Locate and identify every blood parasite.
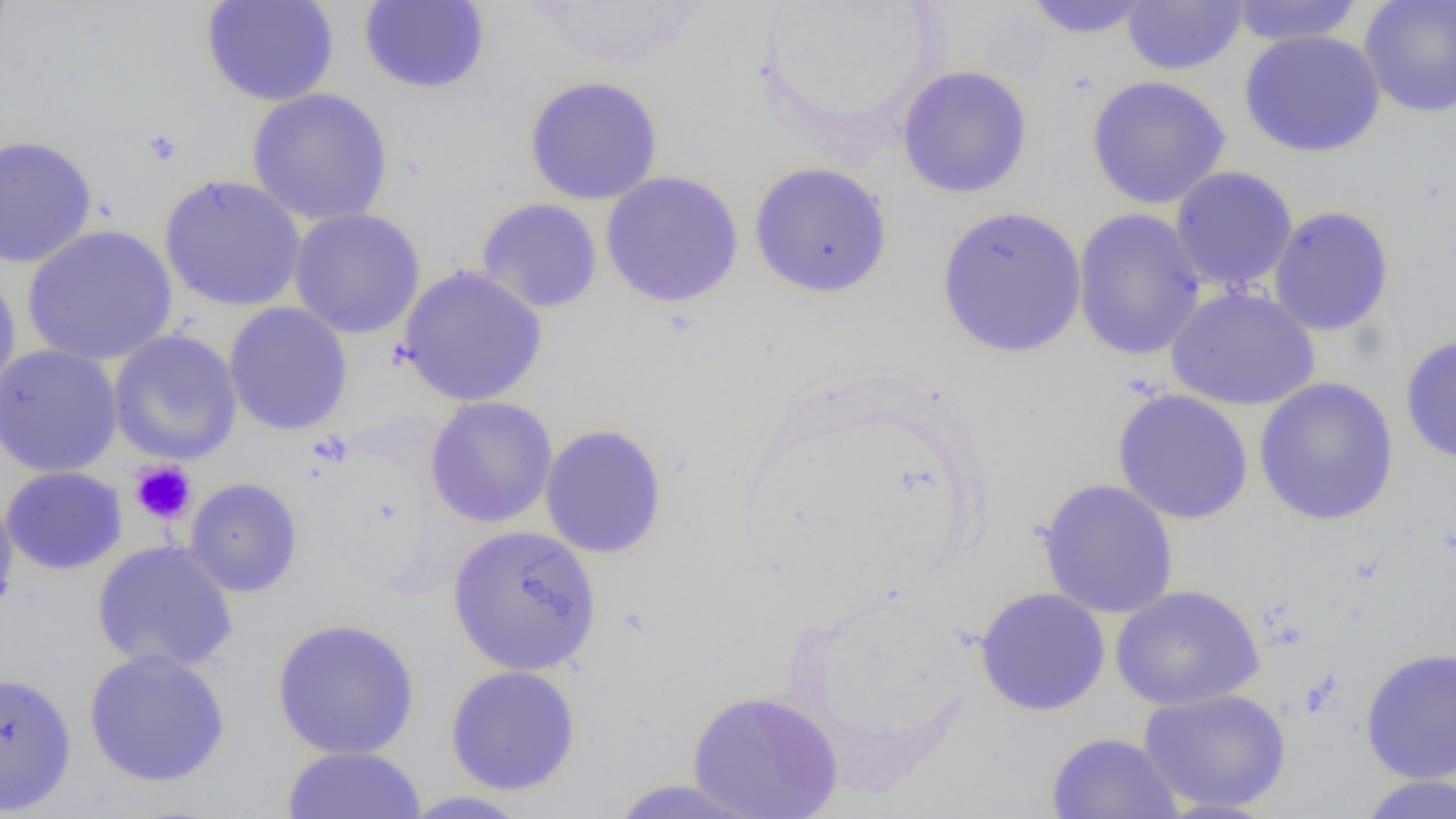
No blood parasites observed.

Approximate bounding boxes as named x1/y1/x2/y2 corners in pixels. Platelet locations (subset): (x1=141, y1=129, x2=183, y2=167), (x1=129, y1=460, x2=197, y2=525). Uninfected red blood cell locations (subset): (x1=0, y1=0, x2=14, y2=60), (x1=200, y1=0, x2=339, y2=107), (x1=752, y1=0, x2=945, y2=155), (x1=1020, y1=0, x2=1158, y2=39), (x1=358, y1=1, x2=491, y2=95), (x1=525, y1=1, x2=714, y2=71), (x1=1121, y1=1, x2=1247, y2=75), (x1=1225, y1=1, x2=1366, y2=46), (x1=1359, y1=1, x2=1456, y2=118), (x1=1239, y1=29, x2=1386, y2=158), (x1=895, y1=65, x2=1034, y2=199), (x1=523, y1=75, x2=664, y2=206), (x1=1086, y1=75, x2=1231, y2=210), (x1=246, y1=87, x2=394, y2=227), (x1=0, y1=134, x2=98, y2=269), (x1=749, y1=161, x2=893, y2=299), (x1=1169, y1=166, x2=1298, y2=295), (x1=600, y1=171, x2=744, y2=308), (x1=159, y1=173, x2=307, y2=313), (x1=475, y1=197, x2=603, y2=314), (x1=936, y1=205, x2=1087, y2=358), (x1=1267, y1=205, x2=1395, y2=337), (x1=1072, y1=207, x2=1207, y2=361), (x1=287, y1=208, x2=426, y2=339), (x1=21, y1=224, x2=178, y2=366), (x1=0, y1=265, x2=22, y2=406), (x1=398, y1=265, x2=548, y2=407), (x1=1165, y1=286, x2=1321, y2=411), (x1=224, y1=302, x2=353, y2=436), (x1=108, y1=329, x2=244, y2=466), (x1=1399, y1=332, x2=1456, y2=466), (x1=0, y1=344, x2=123, y2=478), (x1=1253, y1=376, x2=1400, y2=527), (x1=1112, y1=388, x2=1254, y2=525), (x1=425, y1=396, x2=559, y2=529), (x1=539, y1=423, x2=668, y2=559), (x1=184, y1=478, x2=303, y2=597), (x1=1036, y1=478, x2=1180, y2=619), (x1=0, y1=488, x2=19, y2=624), (x1=447, y1=524, x2=602, y2=675), (x1=91, y1=540, x2=239, y2=675), (x1=1110, y1=584, x2=1265, y2=711), (x1=974, y1=587, x2=1111, y2=716), (x1=271, y1=617, x2=420, y2=760), (x1=1360, y1=646, x2=1456, y2=784), (x1=83, y1=649, x2=231, y2=788), (x1=445, y1=664, x2=582, y2=796), (x1=0, y1=670, x2=77, y2=815), (x1=1138, y1=687, x2=1292, y2=814), (x1=687, y1=689, x2=844, y2=818), (x1=1045, y1=731, x2=1183, y2=819), (x1=282, y1=746, x2=426, y2=819), (x1=1355, y1=774, x2=1456, y2=819), (x1=605, y1=778, x2=768, y2=819), (x1=399, y1=790, x2=534, y2=818). Slide-level diagnosis: negative for blood parasites. Single field of view. Thin blood smear. Light microscopy. Image is 1456×819 pixels. 1000x magnification.